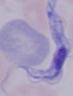
{
  "identification": "trypanosome",
  "modality": "micrograph",
  "magnification": "1000x"
}